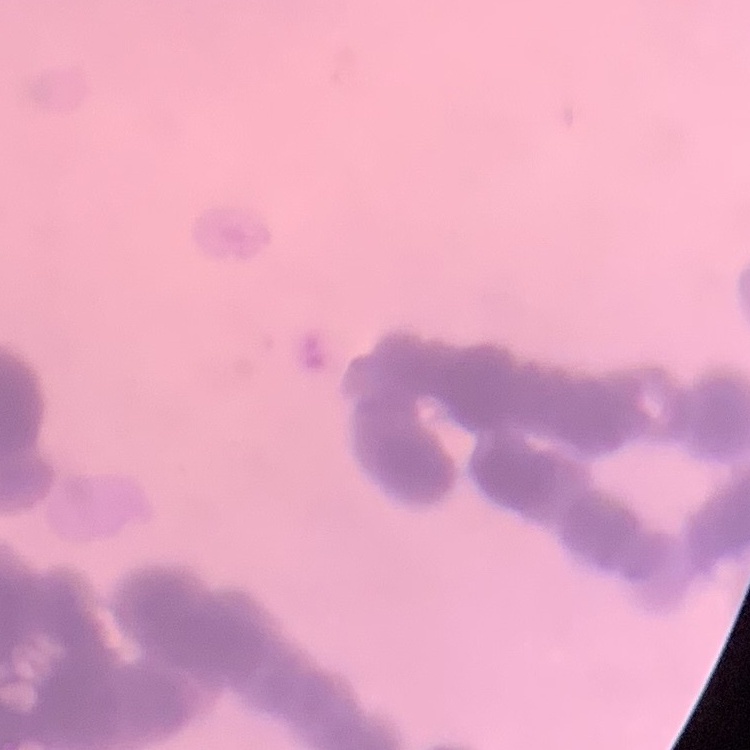 The erythrocytes exhibit rouleaux formation. Thin blood smear. Field's or Giemsa stain. Square crop of a larger photomicrograph.